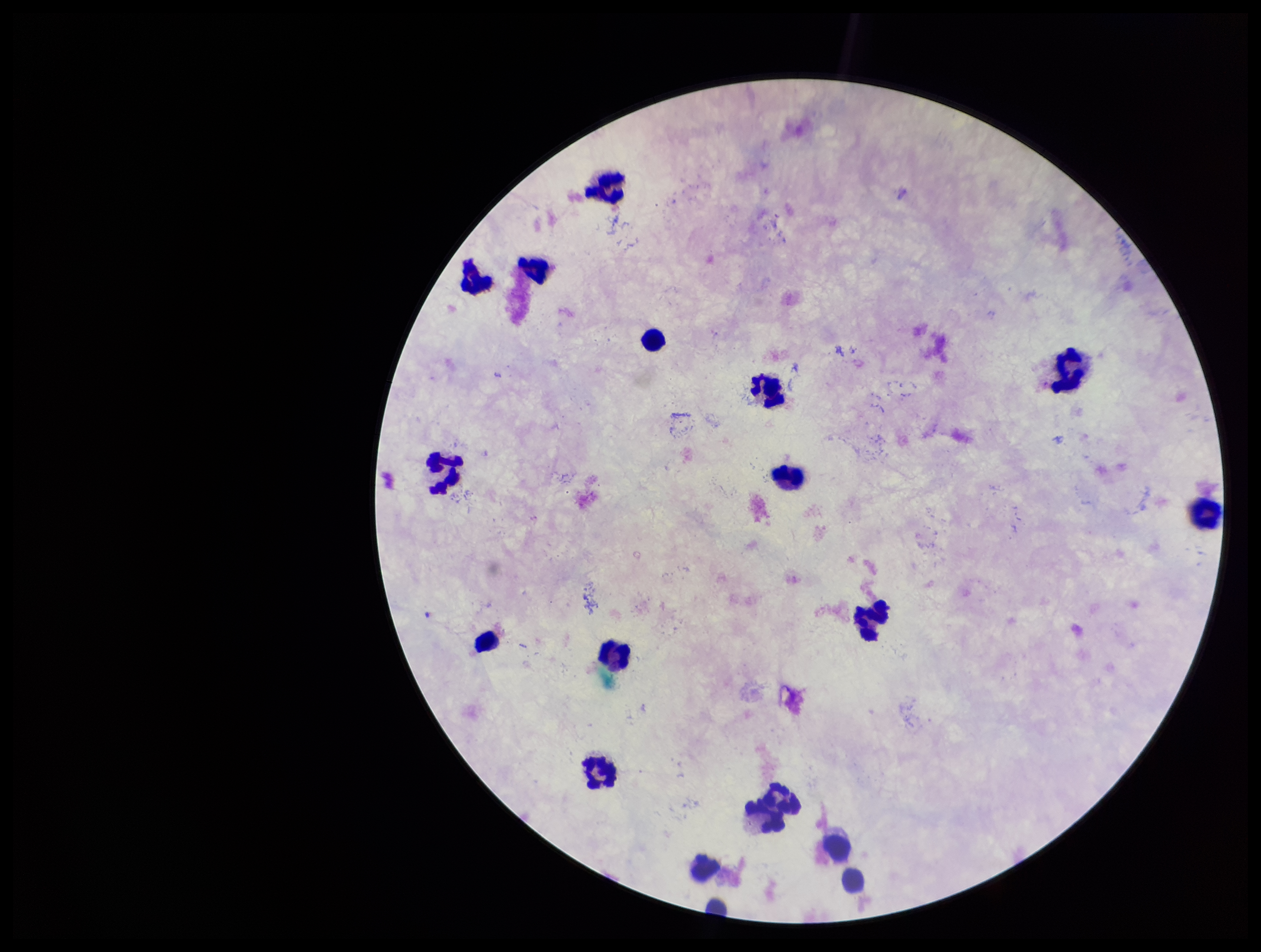
Summary:
  - Patient malaria status: negative
  - Capture: smartphone photograph through the microscope eyepiece
  - Parasite count: 0
  - Field of view: one from this slide
  - Stain: Giemsa
  - Leukocyte count: 17
  - Plasmodium parasites: none seen
  - Preparation: thick
  - Image size: 1261×952 pixels